Locate every malaria parasite.
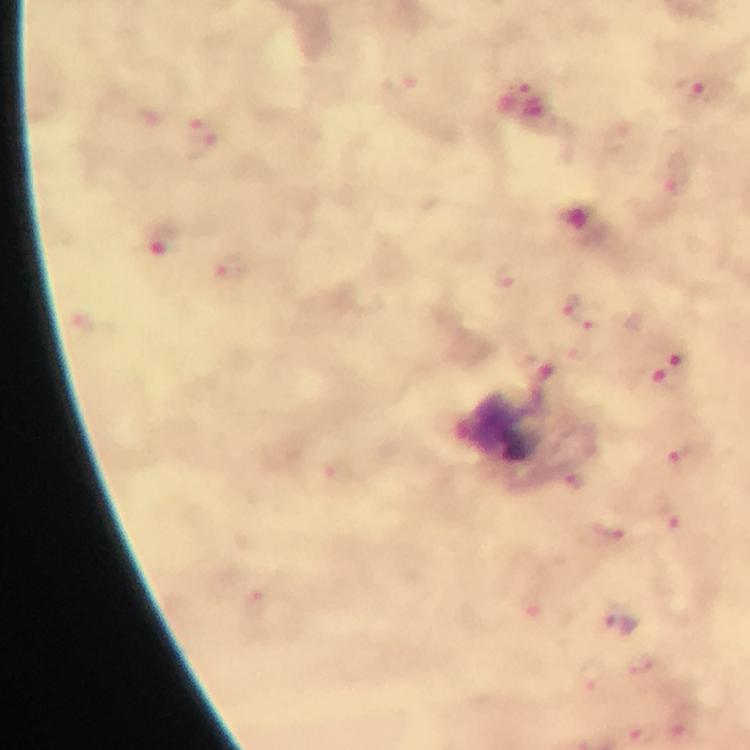
Approximate object centers, in pixels from the top-left corner.
Malaria parasites: (x=695, y=89), (x=204, y=137), (x=677, y=178), (x=161, y=245), (x=232, y=265), (x=508, y=278), (x=570, y=304), (x=590, y=316), (x=678, y=356), (x=672, y=382), (x=689, y=460), (x=575, y=482), (x=672, y=520), (x=610, y=534), (x=620, y=623), (x=644, y=668), (x=683, y=732).

Cropped region of a single field of view. Giemsa-stained preparation. From a diagnostic examination for malaria. Photographed through the microscope with a smartphone camera. Image is 750×750 pixels. At 100x magnification. Immersion oil applied. Thick blood smear.